Classify this cell by malaria status.
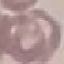
Uninfected.

Giemsa-stained preparation. Thin blood smear. Acquired by smartphone through the microscope eyepiece. Cell patch, automatically extracted from a larger field of view and resized to 64 × 64 pixels.